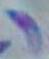

1000x magnification. Toxoplasma gondii is shown. Photomicrograph.